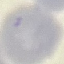

Summary:
  - Result: no malaria parasites seen
  - Stain: Giemsa
  - Image type: cell patch, automatically extracted from a larger field of view and resized to 64 × 64 pixels
  - Preparation: thin blood film
  - Capture: smartphone camera at the microscope eyepiece